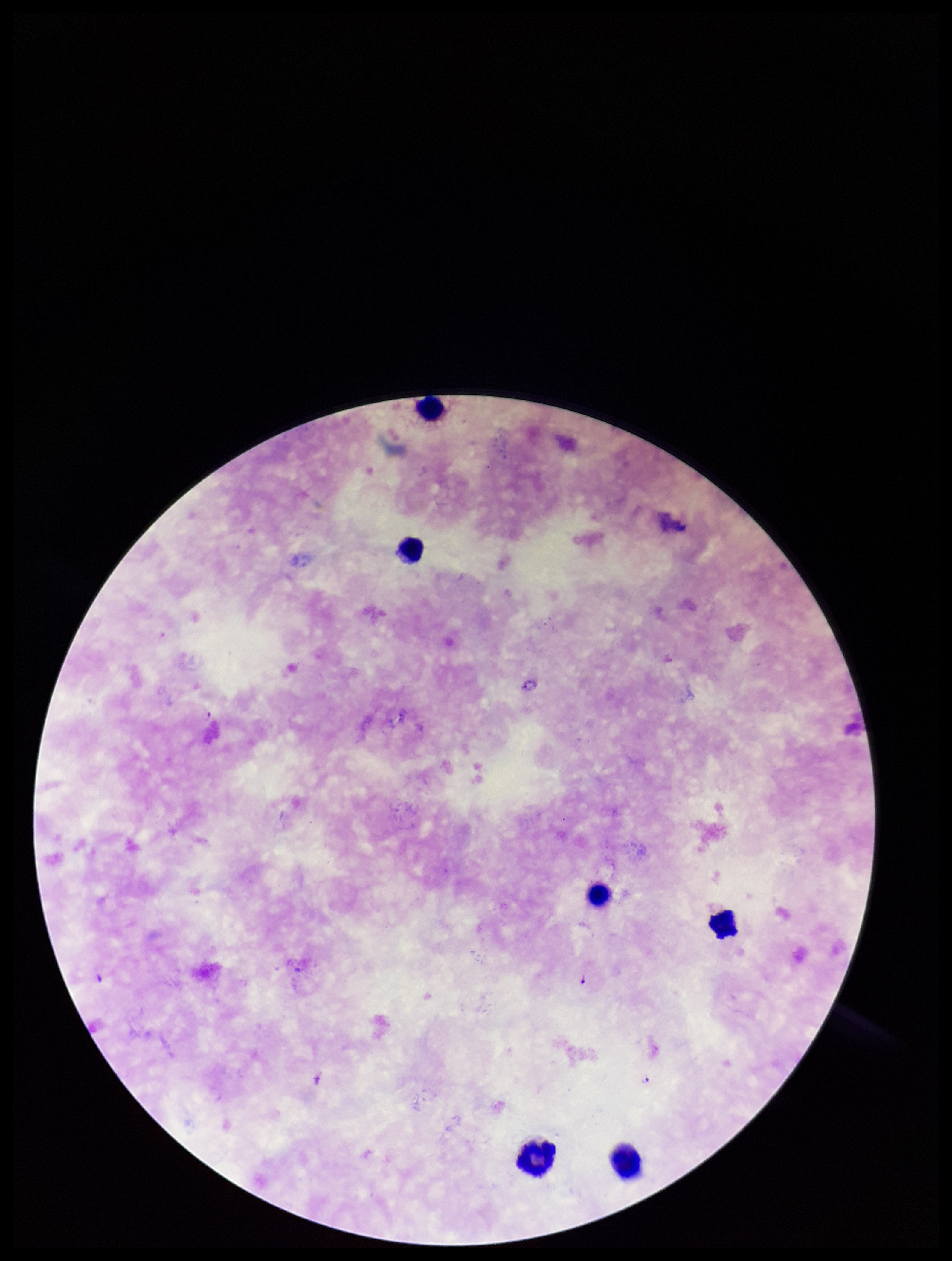
Summary:
  - Image size: 952×1261 pixels
  - Plasmodium parasites: seen
  - Field of view: one from this slide
  - Preparation: thick
  - Patient malaria status: positive
  - Parasite count: 3
  - Leukocyte count: 6
  - Stain: Giemsa
  - Capture: smartphone photograph through the microscope eyepiece
  - Species reported for this patient: Plasmodium falciparum